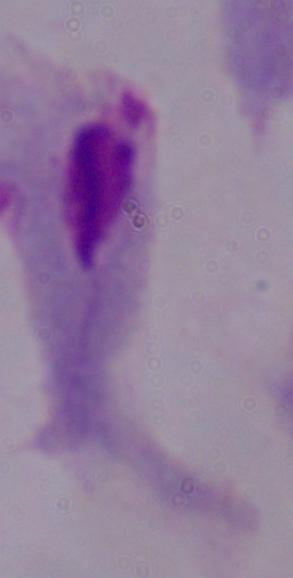
modality: micrograph
magnification: 1000x
identification: trichomonad